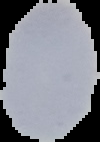
preparation = thin blood film
malaria status = uninfected
image type = segmented cell region on a black background
image size = 100×142 pixels